Give the extent of all Babesia divergens-infected red blood cells.
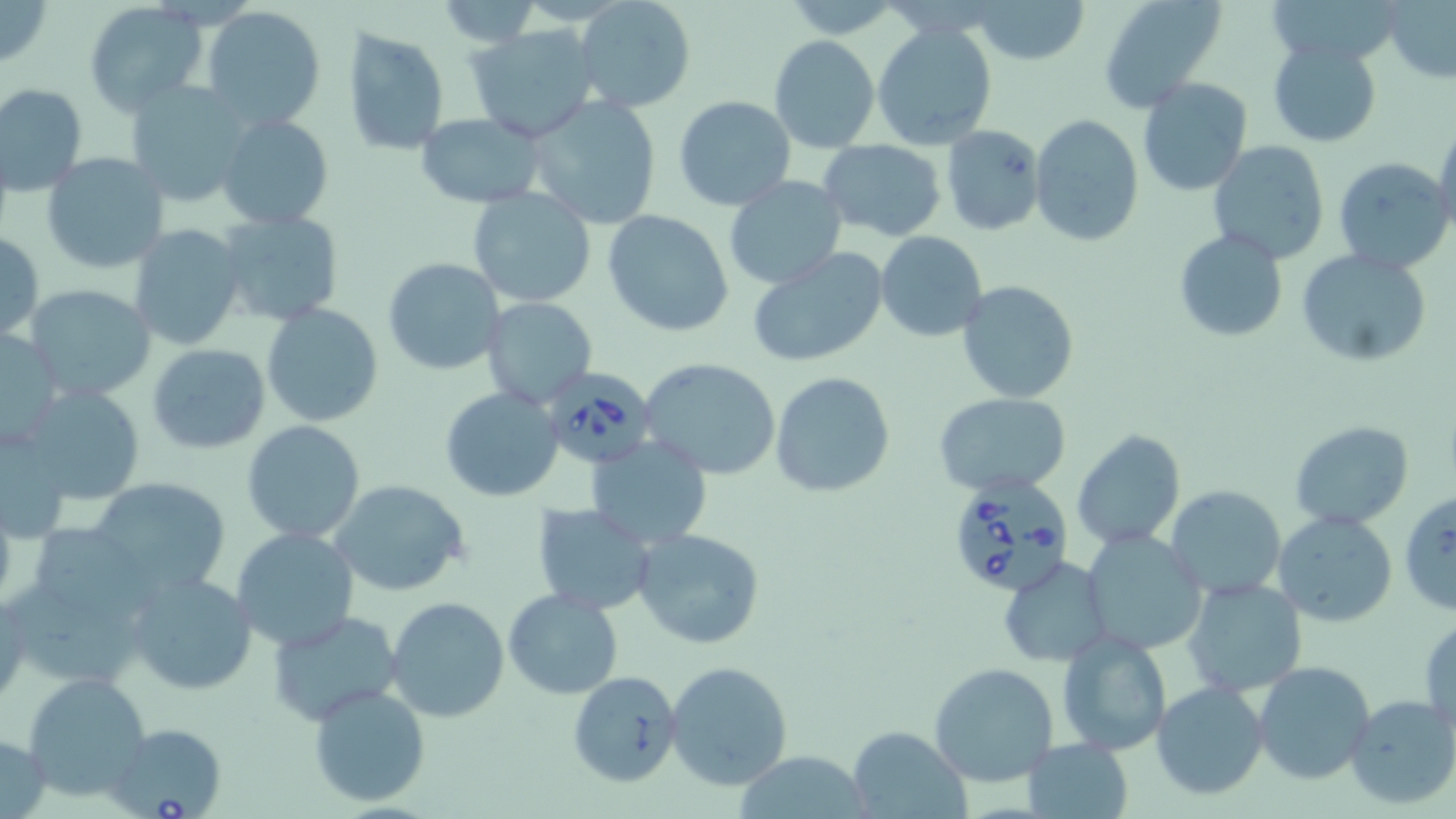
Approximate bounding boxes as (x1, y1, x2, y2) in pixels.
Babesia divergens-infected red blood cells: (537, 365, 657, 473), (950, 476, 1076, 598), (106, 722, 229, 818).

Summary:
  - Uninfected red blood cell locations: (0, 0, 52, 67), (970, 0, 1090, 67), (1098, 0, 1227, 111), (1386, 0, 1455, 85), (429, 1, 546, 46), (574, 1, 699, 115), (82, 2, 209, 115), (201, 6, 328, 131), (872, 22, 998, 151), (466, 24, 599, 142), (341, 27, 450, 157), (770, 35, 879, 152), (1266, 37, 1383, 148), (485, 41, 652, 197), (1137, 78, 1252, 196), (124, 80, 252, 207), (0, 83, 88, 195), (672, 94, 796, 211), (524, 96, 663, 231), (216, 111, 335, 231), (416, 112, 548, 208), (1029, 113, 1144, 247), (941, 125, 1045, 235), (1432, 128, 1456, 241), (818, 140, 946, 240), (1207, 141, 1330, 263), (40, 152, 170, 274), (1332, 156, 1453, 274), (722, 177, 848, 289), (465, 186, 597, 310), (215, 209, 345, 326), (603, 210, 734, 338), (129, 223, 245, 351), (1174, 229, 1289, 343), (0, 232, 45, 343), (876, 232, 989, 343), (745, 246, 889, 368), (903, 246, 1031, 384), (1297, 250, 1432, 368), (383, 257, 505, 374), (956, 280, 1079, 403), (24, 285, 156, 403), (481, 296, 598, 408), (261, 304, 384, 427), (1, 326, 64, 449), (146, 342, 270, 455), (638, 356, 781, 481), (770, 372, 895, 498), (19, 383, 147, 506), (440, 386, 565, 502), (933, 392, 1071, 496), (241, 420, 365, 542), (1289, 420, 1414, 531), (1071, 428, 1186, 550), (586, 435, 712, 550), (87, 476, 231, 597), (596, 476, 736, 617), (329, 480, 469, 597), (1166, 484, 1287, 599), (1398, 488, 1456, 619), (532, 503, 657, 615), (1273, 511, 1396, 627), (43, 526, 157, 625), (231, 526, 360, 650), (632, 527, 765, 648), (1080, 529, 1207, 655), (997, 555, 1110, 668), (124, 571, 258, 695), (1183, 578, 1307, 698), (11, 582, 153, 690), (503, 587, 624, 701), (1, 592, 28, 705), (386, 596, 510, 722), (266, 609, 405, 726), (1420, 616, 1455, 739), (1057, 628, 1172, 754), (665, 662, 794, 791), (1253, 662, 1376, 786), (930, 663, 1060, 786), (20, 670, 153, 801), (567, 670, 682, 787), (1152, 681, 1271, 802), (306, 683, 431, 809), (1345, 693, 1456, 811), (846, 729, 969, 817), (0, 732, 52, 818), (1025, 737, 1133, 817), (731, 751, 873, 818)
  - Slide-level diagnosis: Babesia divergens
  - Preparation: thin blood film
  - Field of view: one of a larger specimen
  - Modality: optical microscopy
  - Image size: 1456×819 pixels
  - Stain: May-Grünwald-Giemsa
  - Magnification: 1000x